State the blood parasite species.
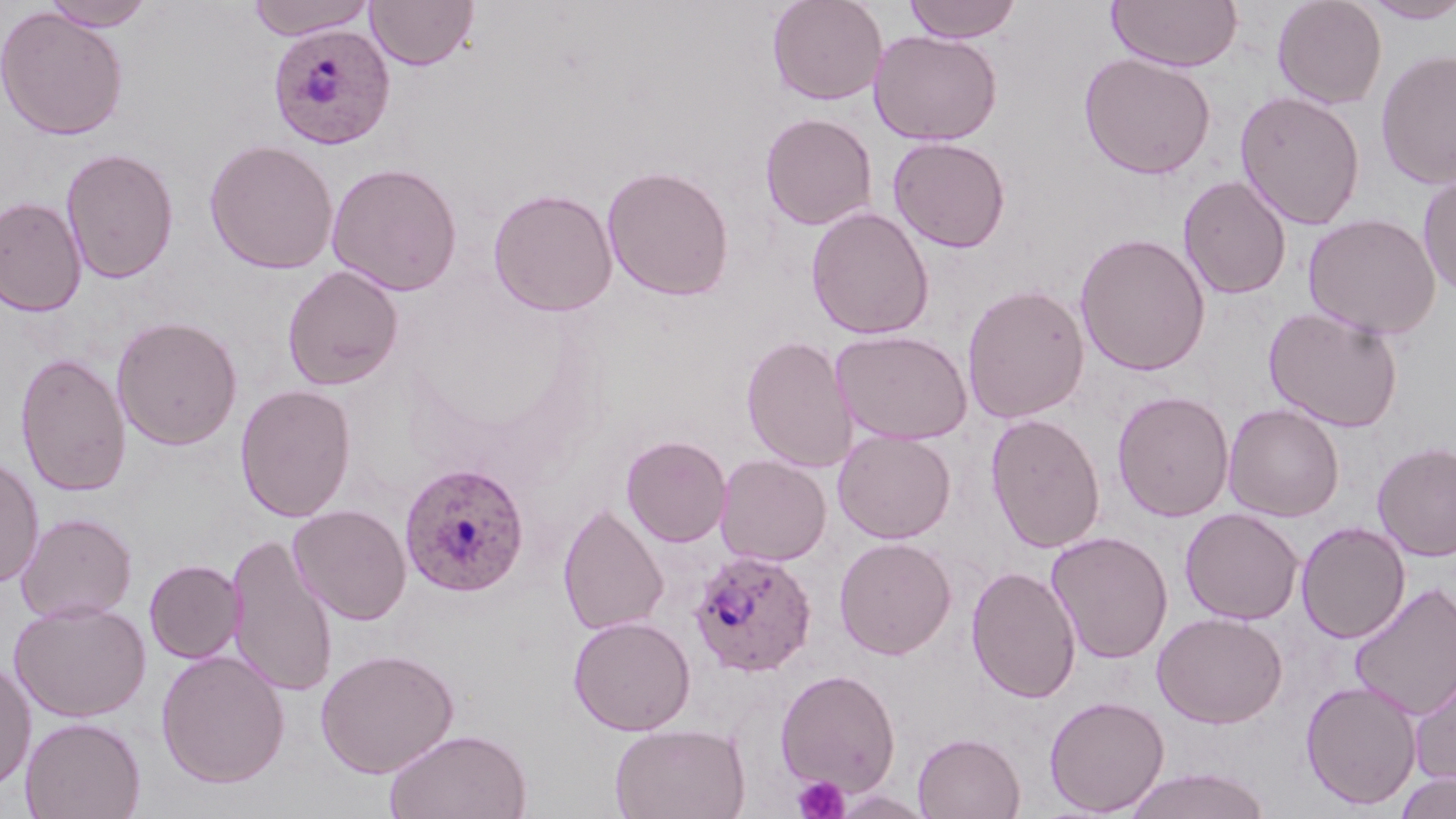
Plasmodium ovale.

image size = 1456×819 pixels
uninfected red blood cell locations = approximate bounding boxes as (x1,y1)-(x2,y2) corner pairs in pixels: (42,0)-(156,31), (245,0)-(377,40), (365,0)-(479,71), (767,0)-(888,106), (902,0)-(1023,43), (1107,0)-(1243,72), (1271,0)-(1387,109), (1360,1)-(1456,23), (0,7)-(129,141), (869,29)-(1003,146), (1375,49)-(1456,190), (1078,52)-(1216,180), (1234,89)-(1366,230), (759,111)-(878,231), (888,135)-(1011,253), (204,139)-(339,274), (60,147)-(179,284), (326,161)-(463,296), (602,165)-(735,301), (1418,173)-(1456,301), (1178,175)-(1292,299), (488,188)-(618,316), (0,196)-(87,317), (806,207)-(934,340), (1302,213)-(1442,340), (1074,232)-(1211,376), (282,264)-(405,391), (962,283)-(1090,423), (1263,305)-(1404,433), (112,315)-(243,450), (832,329)-(973,445), (741,335)-(858,472), (16,353)-(132,497), (235,384)-(356,522), (1112,390)-(1234,522), (1223,403)-(1345,522), (985,413)-(1106,554), (832,429)-(956,544), (621,435)-(732,547), (1371,441)-(1456,561), (714,446)-(957,559), (715,453)-(832,566), (0,455)-(44,589), (289,504)-(412,624), (558,504)-(669,636), (1180,508)-(1304,625), (15,512)-(137,624), (1295,521)-(1409,643), (1046,530)-(1173,664), (225,533)-(338,699), (833,536)-(957,660), (144,559)-(245,663), (967,565)-(1081,703), (1348,581)-(1456,721), (8,599)-(151,722), (1152,611)-(1287,728), (568,615)-(696,736), (315,647)-(459,778), (155,650)-(291,788), (0,658)-(36,791), (1409,663)-(1456,790), (775,668)-(901,796), (1300,679)-(1423,810), (1044,694)-(1170,816), (20,715)-(146,819), (610,722)-(751,819), (384,728)-(533,818), (913,732)-(1025,819), (1121,767)-(1273,819), (1393,772)-(1456,819)
modality = light microscopy
Plasmodium ovale-infected red blood cell locations = approximate bounding boxes as (x1,y1)-(x2,y2) corner pairs in pixels: (268,24)-(396,149), (399,461)-(529,598), (688,548)-(817,678)
preparation = thin blood smear
platelet locations = approximate bounding boxes as (x1,y1)-(x2,y2) corner pairs in pixels: (792,776)-(850,819)
field of view = single
magnification = 1000x
stain = May-Grünwald-Giemsa